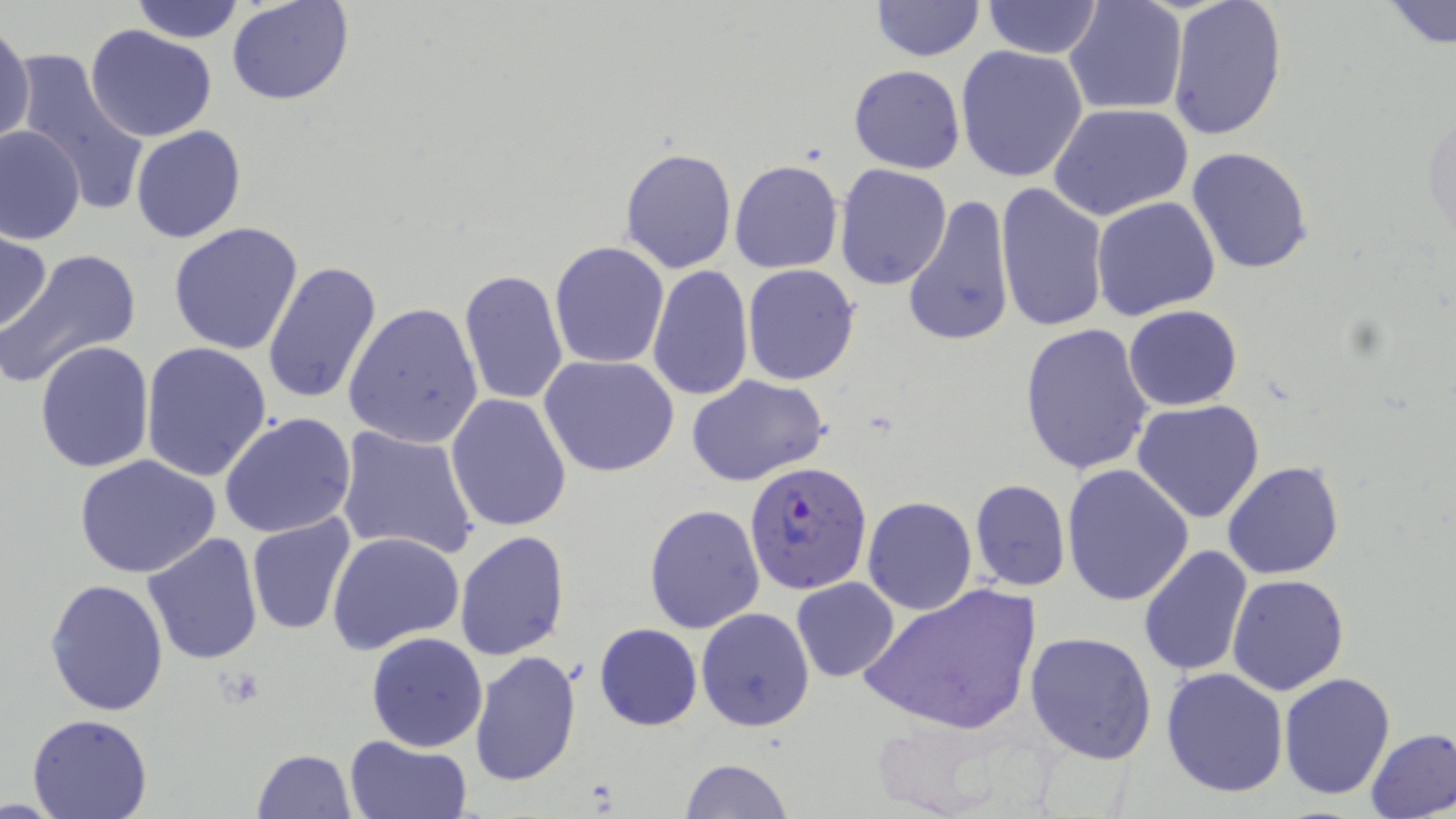

slide-level diagnosis = Plasmodium falciparum
modality = light microscopy
Plasmodium falciparum-infected red blood cell locations = approximate bounding boxes as named x1/y1/x2/y2 corners in pixels: (x1=744, y1=462, x2=872, y2=596)
stain = May-Grünwald-Giemsa
field of view = one of a larger specimen
magnification = 1000x
image size = 1456×819 pixels
uninfected red blood cell locations = approximate bounding boxes as named x1/y1/x2/y2 corners in pixels: (x1=129, y1=0, x2=248, y2=44), (x1=227, y1=0, x2=354, y2=106), (x1=870, y1=0, x2=983, y2=61), (x1=980, y1=0, x2=1104, y2=57), (x1=1064, y1=0, x2=1188, y2=117), (x1=1166, y1=1, x2=1288, y2=143), (x1=1383, y1=1, x2=1456, y2=50), (x1=0, y1=21, x2=35, y2=149), (x1=85, y1=26, x2=218, y2=143), (x1=954, y1=44, x2=1089, y2=183), (x1=7, y1=48, x2=152, y2=215), (x1=848, y1=65, x2=966, y2=174), (x1=1049, y1=103, x2=1194, y2=221), (x1=1424, y1=106, x2=1455, y2=246), (x1=1, y1=124, x2=85, y2=244), (x1=130, y1=126, x2=245, y2=243), (x1=619, y1=145, x2=737, y2=274), (x1=1186, y1=147, x2=1314, y2=276), (x1=729, y1=159, x2=844, y2=274), (x1=834, y1=164, x2=952, y2=288), (x1=993, y1=181, x2=1108, y2=332), (x1=902, y1=193, x2=1016, y2=348), (x1=1092, y1=195, x2=1221, y2=321), (x1=168, y1=222, x2=305, y2=357), (x1=0, y1=231, x2=53, y2=335), (x1=550, y1=241, x2=671, y2=369), (x1=1, y1=246, x2=143, y2=391), (x1=261, y1=260, x2=384, y2=405), (x1=742, y1=263, x2=861, y2=386), (x1=647, y1=265, x2=754, y2=399), (x1=459, y1=269, x2=570, y2=407), (x1=344, y1=302, x2=483, y2=449), (x1=1123, y1=305, x2=1244, y2=412), (x1=1019, y1=323, x2=1155, y2=476), (x1=34, y1=341, x2=155, y2=473), (x1=141, y1=342, x2=272, y2=483), (x1=539, y1=354, x2=680, y2=477), (x1=686, y1=375, x2=831, y2=487), (x1=445, y1=393, x2=573, y2=534), (x1=1131, y1=400, x2=1265, y2=524), (x1=219, y1=413, x2=357, y2=540), (x1=336, y1=424, x2=481, y2=560), (x1=73, y1=453, x2=221, y2=579), (x1=1222, y1=461, x2=1345, y2=581), (x1=1062, y1=464, x2=1195, y2=607), (x1=969, y1=478, x2=1071, y2=592), (x1=863, y1=495, x2=978, y2=615), (x1=644, y1=503, x2=765, y2=633), (x1=245, y1=512, x2=358, y2=637), (x1=454, y1=530, x2=571, y2=662), (x1=327, y1=531, x2=466, y2=655), (x1=142, y1=532, x2=266, y2=667), (x1=1137, y1=546, x2=1254, y2=680), (x1=1227, y1=573, x2=1348, y2=694), (x1=791, y1=577, x2=900, y2=682), (x1=43, y1=578, x2=169, y2=718), (x1=859, y1=582, x2=1041, y2=736), (x1=695, y1=607, x2=814, y2=732), (x1=594, y1=623, x2=703, y2=732), (x1=366, y1=631, x2=487, y2=751), (x1=1024, y1=631, x2=1157, y2=764), (x1=468, y1=650, x2=584, y2=789), (x1=1161, y1=667, x2=1290, y2=798), (x1=1279, y1=672, x2=1396, y2=799), (x1=28, y1=714, x2=151, y2=819), (x1=1365, y1=727, x2=1456, y2=819), (x1=343, y1=736, x2=473, y2=819), (x1=249, y1=749, x2=357, y2=819), (x1=680, y1=758, x2=795, y2=818)
preparation = thin blood film